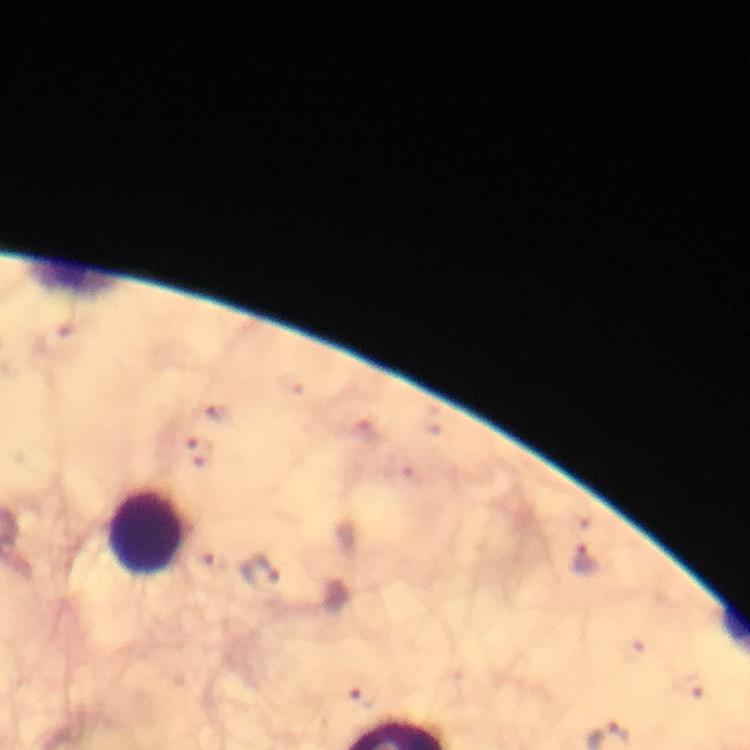

immersion oil = used
cropped from = one field of view
stain = Giemsa
magnification = 100x
capture = smartphone photograph through a microscope
image size = 750×750 pixels
preparation = thick blood smear
malaria parasite locations = approximate object centers, in pixels from the top-left corner: (x=202, y=451), (x=584, y=560), (x=258, y=573), (x=364, y=695)
context = from a diagnostic examination for malaria
leukocyte locations = approximate object centers, in pixels from the top-left corner: (x=145, y=533)